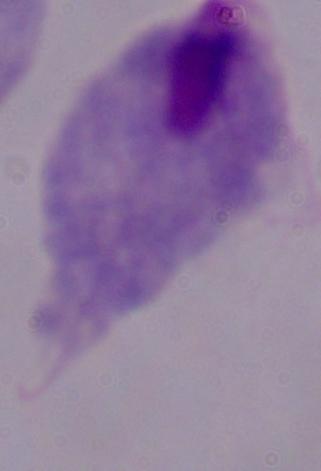

A trichomonad is shown. Photomicrograph. Captured at 1000x magnification.